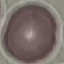
Result: negative for malaria parasites. Photographed with a smartphone camera at the microscope eyepiece. Thin blood film. Cell patch, automatically extracted from a larger field of view and resized to 64 × 64 pixels. Giemsa stain.